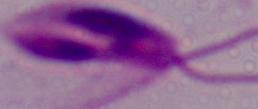

modality: micrograph
identification: Leishmania
magnification: 1000x